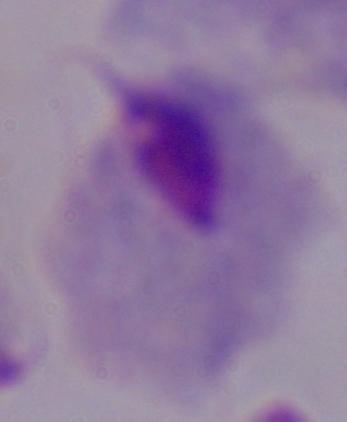

Summary:
  - Magnification: 1000x
  - Modality: micrograph
  - Identification: trichomonad